Assess the morphology of the erythrocytes.
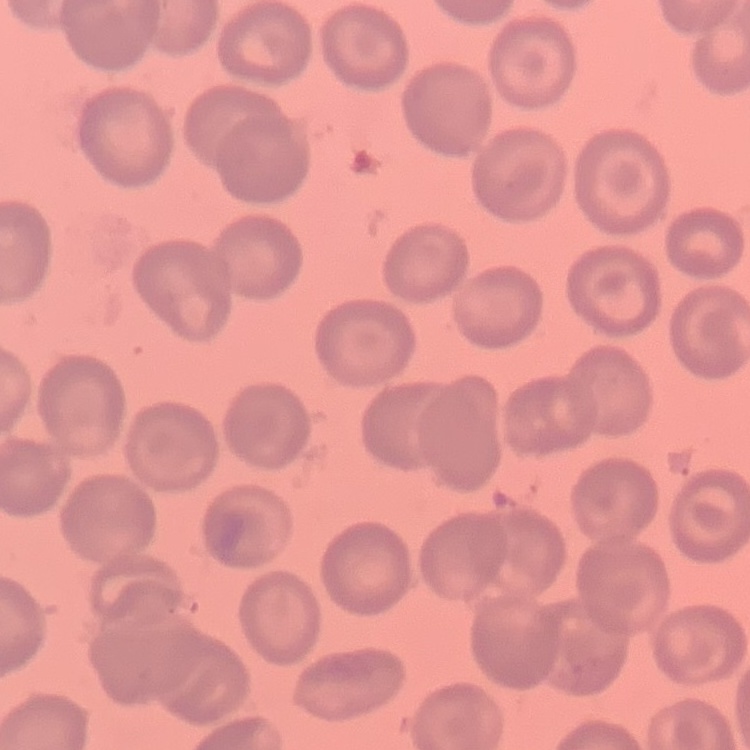

They show no rouleaux formation.

One tile cut from a larger photomicrograph. Thin blood film. Field's or Giemsa stain.